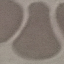
Summary:
  - Result: no malaria parasites detected
  - Preparation: thin blood film
  - Capture: smartphone camera at the microscope eyepiece
  - Image type: cell patch, automatically extracted from a larger field of view and resized to 64 × 64 pixels
  - Stain: Giemsa